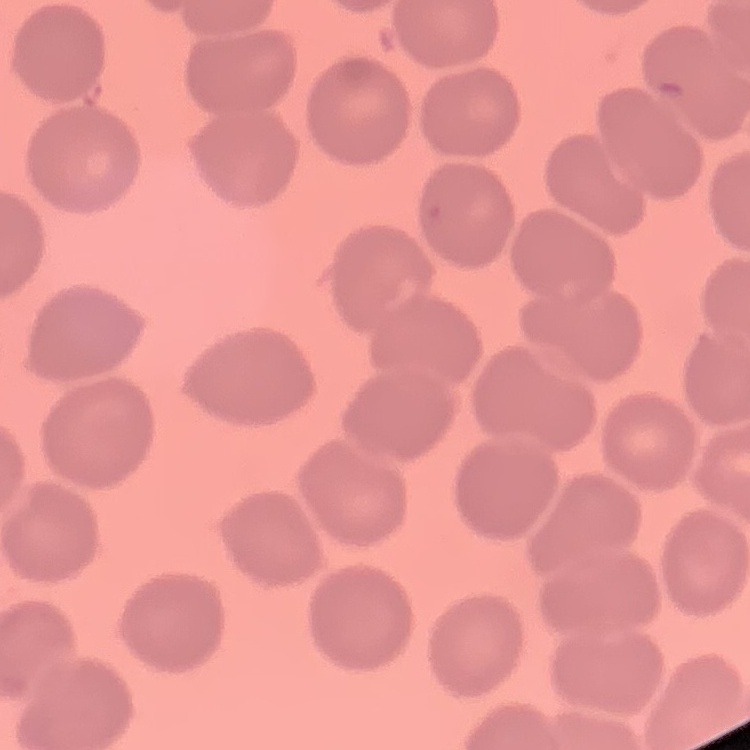
Summary:
  - Erythrocyte morphology: no rouleaux formation
  - Stain: Field's or Giemsa
  - Image type: square crop of a larger photomicrograph
  - Preparation: thin blood smear